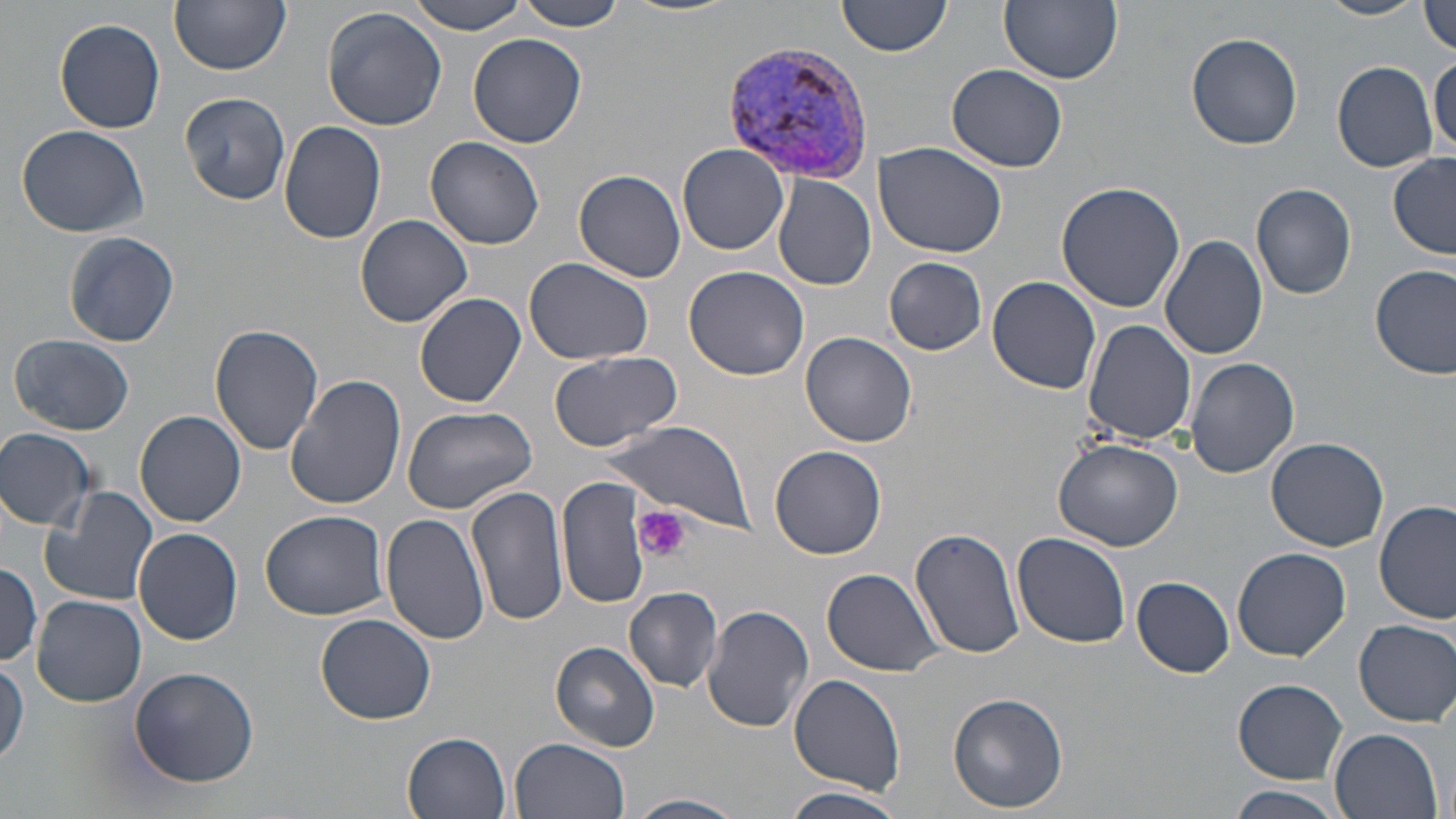
slide_level_diagnosis: Plasmodium vivax
modality: light microscopy
platelet_locations: 'approximate bounding boxes as (x1,y1)-(x2,y2) corner pairs in pixels: (634,506)-(691,563)'
magnification: 1000x
preparation: thin blood film
plasmodium_vivax_infected_red_blood_cell_locations: 'approximate bounding boxes as (x1,y1)-(x2,y2) corner pairs in pixels: (719,39)-(880,184)'
uninfected_red_blood_cell_locations: 'approximate bounding boxes as (x1,y1)-(x2,y2) corner pairs in pixels: (169,0)-(291,74), (404,0)-(529,33), (510,0)-(630,31), (622,0)-(739,17), (838,0)-(951,57), (1000,0)-(1123,85), (1316,0)-(1426,22), (1419,1)-(1456,56), (322,6)-(449,132), (54,17)-(166,132), (467,32)-(588,148), (1185,32)-(1303,150), (1429,54)-(1455,158), (1331,62)-(1438,173), (947,64)-(1069,172), (178,91)-(293,206), (278,120)-(388,245), (17,123)-(148,238), (425,136)-(545,251), (874,141)-(1008,258), (677,144)-(790,255), (1388,152)-(1456,259), (573,169)-(687,282), (773,175)-(877,291), (1251,182)-(1357,299), (1055,183)-(1187,315), (354,214)-(472,328), (62,230)-(179,348), (1159,233)-(1267,361), (885,257)-(987,354), (525,258)-(654,366), (684,265)-(809,381), (1371,265)-(1456,381), (986,276)-(1102,395), (415,292)-(527,407), (1083,320)-(1196,445), (210,323)-(325,457), (801,331)-(917,447), (9,333)-(136,436), (549,350)-(682,451), (1185,357)-(1299,478), (285,375)-(405,511), (402,405)-(537,515), (135,411)-(246,527), (601,421)-(754,530), (0,428)-(97,531), (1266,437)-(1390,550), (1055,438)-(1184,550), (772,446)-(887,560), (558,475)-(648,611), (467,484)-(571,628), (40,485)-(158,608), (1375,501)-(1455,625), (260,509)-(389,621), (380,513)-(491,645), (910,526)-(1024,659), (134,528)-(243,645), (1011,534)-(1131,648), (1231,547)-(1351,660), (0,563)-(44,666), (821,567)-(945,677), (1133,578)-(1235,677), (624,586)-(723,691), (31,595)-(146,706), (702,603)-(814,733), (314,614)-(436,724), (1354,618)-(1456,727), (550,640)-(661,751), (0,659)-(28,768), (129,665)-(260,786), (788,671)-(906,794), (1233,679)-(1348,783), (948,690)-(1069,812), (1330,728)-(1443,819), (403,731)-(512,817), (511,736)-(631,819), (1229,786)-(1343,819), (782,787)-(906,819), (627,793)-(746,819)'
stain: May-Grünwald-Giemsa
image_size: 1456×819 pixels
field_of_view: one of a larger specimen